Assess this cell for malaria.
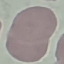
Uninfected.

capture = smartphone through the microscope eyepiece
image type = cell patch, automatically extracted from a larger field of view and resized to 64 × 64 pixels
preparation = thin blood smear
stain = Giemsa